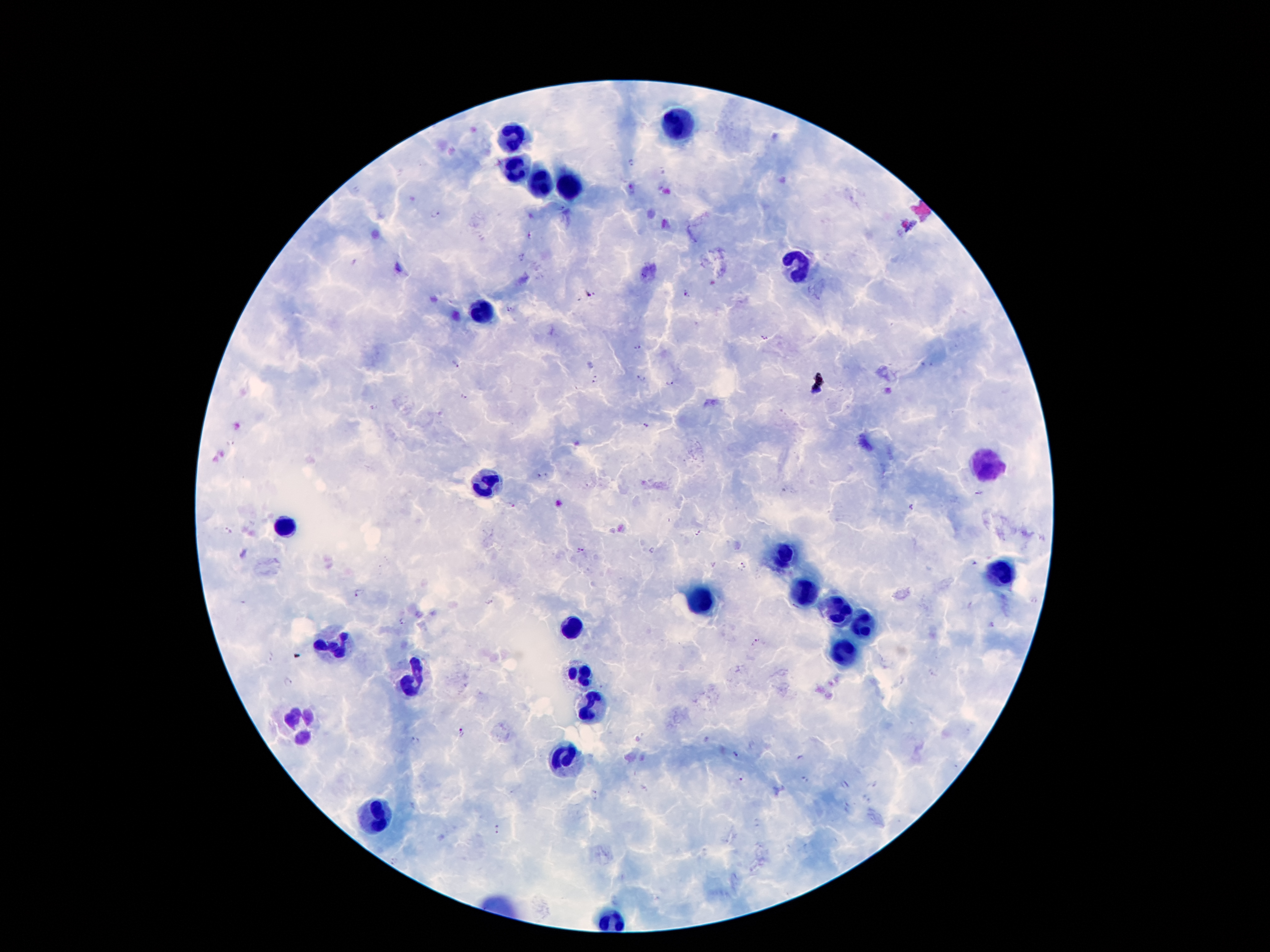
stain: Giemsa
image_size: 1270×952 pixels
leukocyte_locations: 'approximate centers as [x, y] in pixels: [679, 124], [513, 137], [515, 169], [538, 188], [573, 188], [798, 264], [482, 313], [984, 468], [482, 485], [281, 528], [784, 556], [1001, 573], [802, 595], [698, 602], [831, 606], [859, 624], [573, 630], [333, 645], [845, 649], [579, 675], [415, 679], [591, 706], [298, 720], [562, 759], [378, 815]'
magnification: 100x
preparation: thick blood film
capture: smartphone camera through the microscope eyepiece
malaria_parasite_locations: 'approximate centers as [x, y] in pixels: [631, 163], [434, 213], [530, 234], [523, 258], [687, 293], [588, 294], [510, 308], [764, 337], [636, 346], [454, 364], [640, 378], [595, 380], [668, 382], [465, 396], [373, 407], [646, 424], [230, 443], [540, 475], [979, 492], [910, 508], [228, 531], [697, 531], [580, 550], [741, 566], [358, 594], [1034, 600], [401, 621], [756, 642], [270, 657], [933, 671], [288, 681], [463, 731], [414, 741], [737, 754], [804, 779], [740, 780], [844, 785], [595, 792], [497, 829]'
field_of_view: one from this slide
patient_malaria_status: infected with Plasmodium falciparum